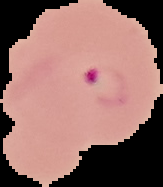

image type = cell region segmented out of the field of view; surrounding area masked to black
image size = 163×187 pixels
preparation = thin blood smear
malaria status = parasitized